Point out each malaria parasite.
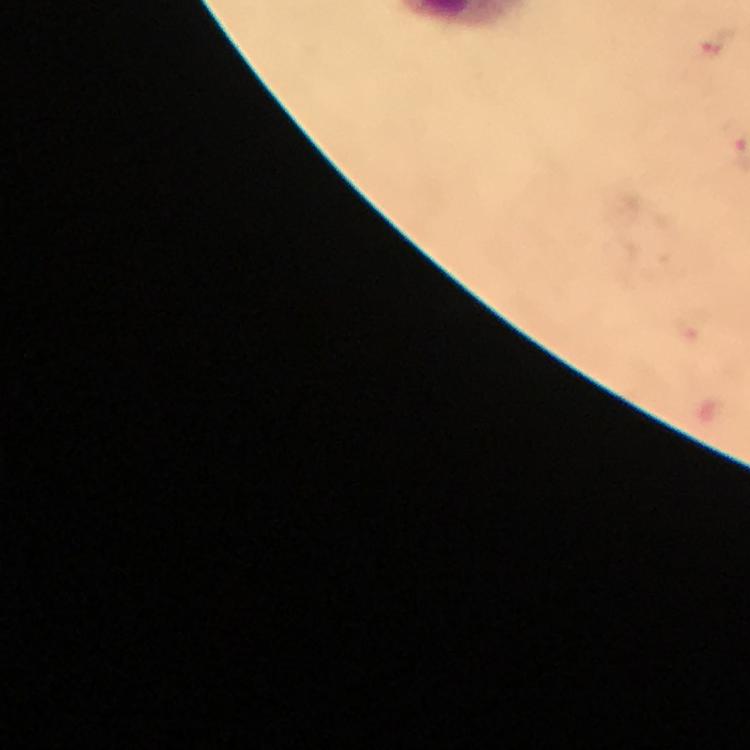
Approximate centers as [x, y] in pixels.
Malaria parasites: [714, 42].

image_size: 750×750 pixels
cropped_from: a single field of view
magnification: 100x
context: from a malaria diagnostic workup
stain: Giemsa
preparation: thick smear
capture: smartphone photograph through a microscope
immersion_oil: used